State which parasite is depicted.
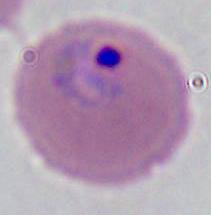

Plasmodium.

400x or 1000x magnification. Micrograph.